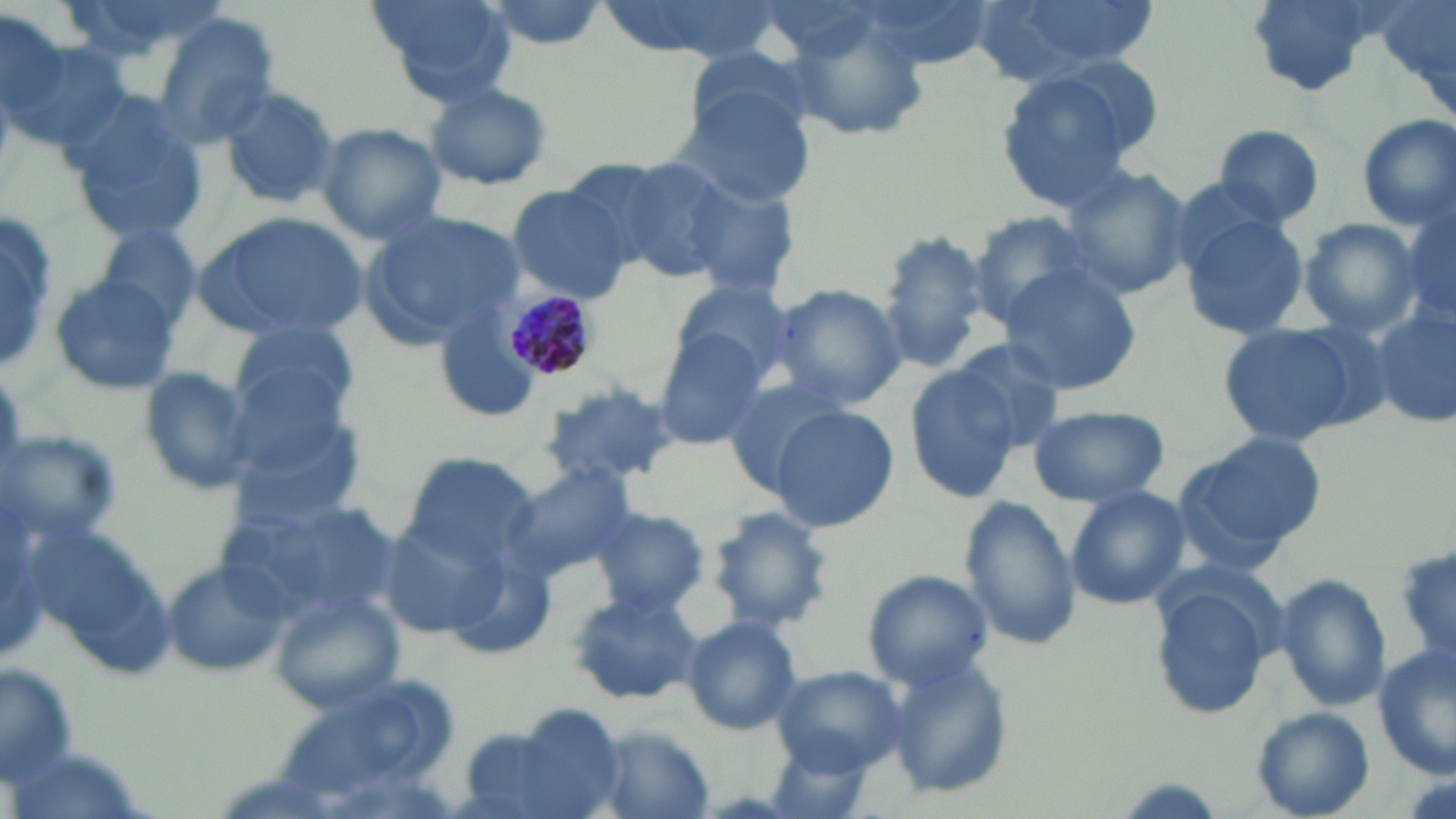
Approximate bounding boxes as [x1, y1, x2, y2] in pixels. Uninfected red blood cell locations: [368, 0, 517, 105], [595, 0, 791, 64], [851, 0, 991, 72], [965, 0, 1158, 84], [1378, 0, 1456, 125], [0, 17, 128, 160], [146, 17, 283, 154], [780, 17, 933, 143], [679, 44, 826, 150], [1037, 52, 1167, 160], [995, 73, 1145, 211], [423, 82, 555, 191], [217, 84, 343, 208], [676, 84, 820, 207], [63, 95, 207, 246], [1355, 114, 1456, 231], [316, 122, 448, 244], [1212, 124, 1325, 229], [604, 154, 741, 281], [1056, 162, 1190, 300], [678, 177, 804, 302], [507, 185, 633, 301], [0, 207, 57, 375], [1179, 211, 1311, 339], [194, 212, 366, 342], [358, 212, 520, 349], [968, 212, 1103, 325], [1404, 215, 1455, 323], [0, 217, 60, 375], [1297, 218, 1423, 337], [93, 225, 203, 336], [875, 230, 990, 370], [996, 266, 1141, 396], [47, 275, 181, 397], [669, 279, 800, 386], [768, 283, 909, 410], [1367, 305, 1456, 429], [433, 312, 543, 425], [228, 318, 362, 430], [1216, 320, 1367, 449], [651, 332, 770, 450], [938, 337, 1068, 458], [903, 364, 1031, 503], [136, 367, 260, 497], [718, 373, 851, 496], [539, 384, 682, 493], [221, 398, 372, 530], [1026, 404, 1169, 508], [770, 406, 900, 532], [0, 430, 125, 546], [1177, 434, 1325, 557], [400, 451, 540, 568], [506, 462, 638, 579], [1064, 485, 1190, 610], [216, 488, 396, 624], [0, 489, 50, 667], [958, 495, 1083, 652], [590, 505, 710, 616], [708, 506, 836, 634], [381, 518, 510, 641], [25, 520, 175, 680], [1393, 544, 1455, 663], [165, 560, 288, 677], [862, 570, 993, 690], [1275, 574, 1391, 713], [1152, 580, 1276, 720], [567, 589, 703, 706], [271, 593, 406, 714], [679, 615, 803, 736], [1371, 645, 1456, 778], [882, 655, 1015, 802], [0, 663, 78, 780], [770, 665, 907, 771], [464, 704, 628, 819], [1252, 707, 1376, 818], [586, 726, 718, 818], [762, 738, 883, 819]. Plasmodium malariae-infected red blood cell locations: [505, 289, 595, 381]. Slide-level diagnosis: Plasmodium malariae. Thin blood film. Captured at 1000x magnification. Image is 1456×819 pixels. May-Grünwald-Giemsa stain. Single field of view. Light microscopy.